Point out each leukocyte.
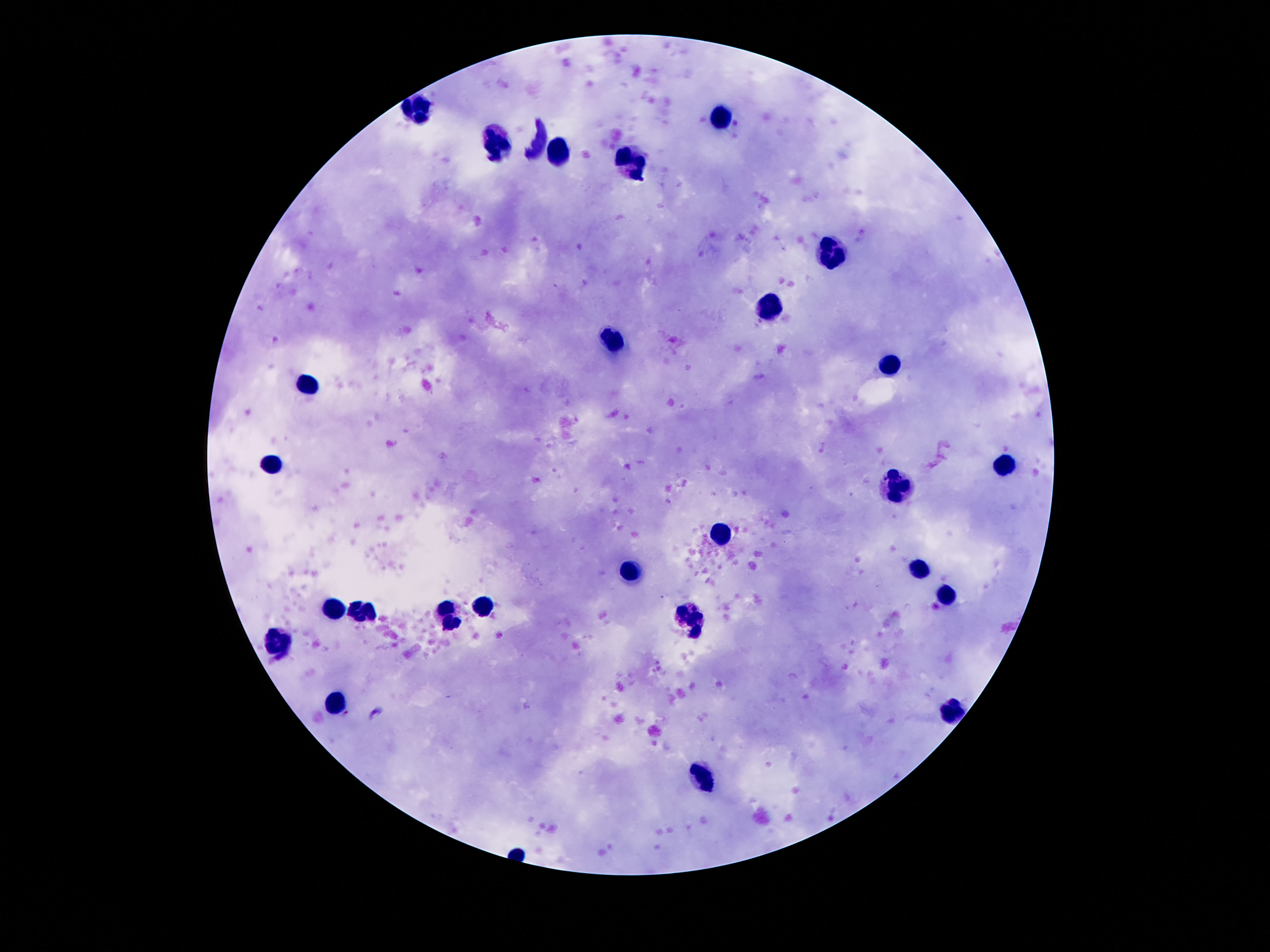

Approximate centers as [x, y] in pixels.
Leukocytes: [417, 106], [722, 117], [498, 145], [557, 155], [632, 164], [831, 250], [768, 307], [614, 340], [890, 366], [308, 383], [1004, 464], [269, 465], [897, 486], [720, 536], [920, 564], [630, 569], [945, 595], [333, 605], [482, 605], [354, 611], [450, 615], [689, 617], [279, 642], [336, 700], [951, 710], [702, 777].

Summary:
  - Capture: smartphone camera through the microscope eyepiece
  - Magnification: 100x
  - Field of view: single
  - Stain: Giemsa
  - Image size: 1270×952 pixels
  - Patient malaria status: not infected
  - Preparation: thick blood smear